Point out each leukocyte.
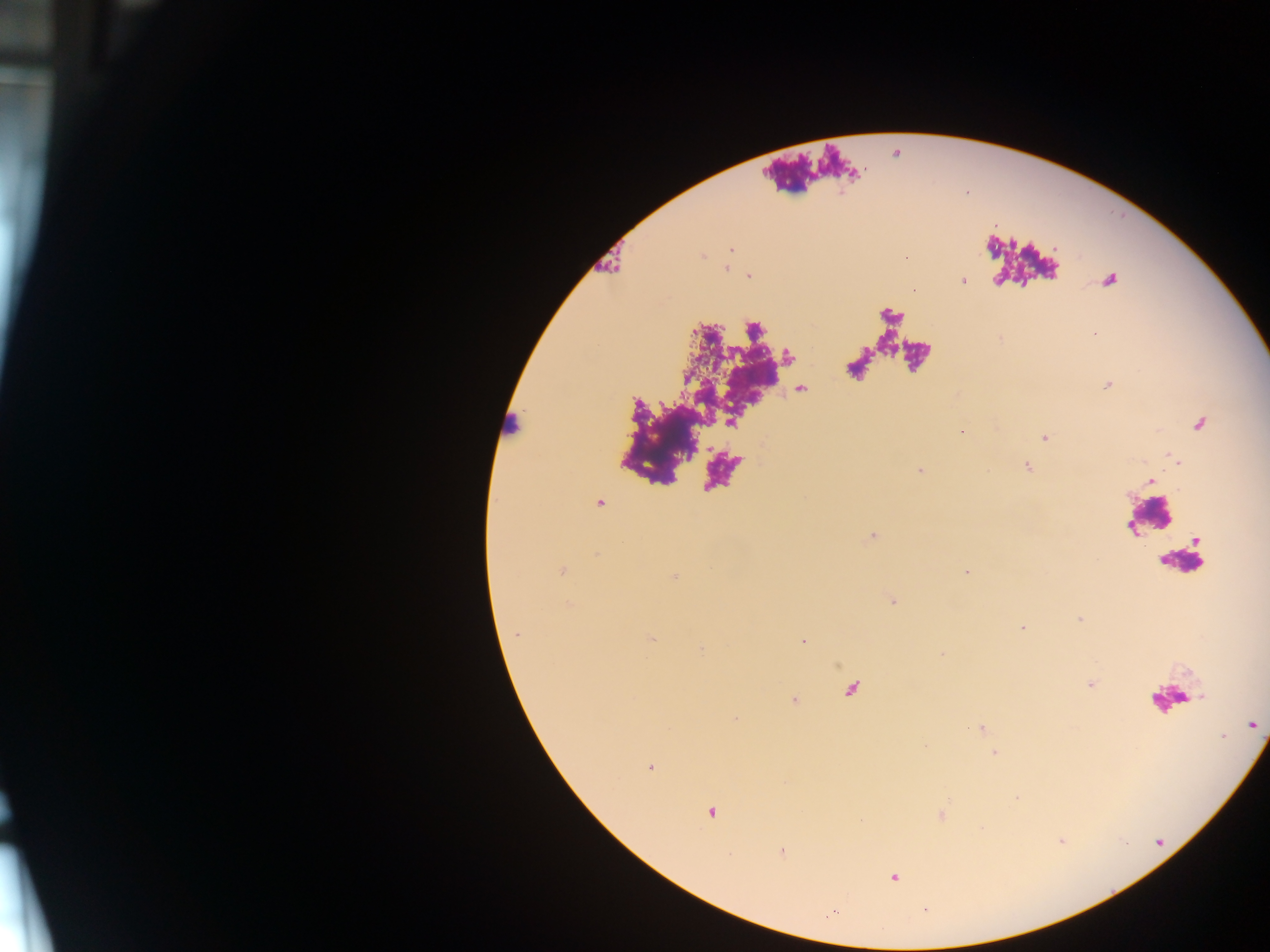

Approximate centers as {x, y} in pixels.
Leukocytes: {512, 427}, {1149, 517}, {1182, 561}, {1169, 699}.

Malaria parasite locations: {731, 248}, {726, 268}, {748, 275}, {962, 280}, {1107, 384}, {1200, 425}, {963, 431}, {1044, 437}, {1026, 466}, {919, 469}, {1150, 479}, {598, 502}, {872, 535}, {562, 571}, {966, 572}, {674, 576}, {892, 600}, {1022, 627}, {651, 638}, {803, 641}, {1091, 684}, {794, 701}, {1252, 724}, {980, 728}, {995, 752}, {650, 767}, {711, 811}, {941, 815}, {781, 851}, {893, 877}, {924, 909}, {833, 910}. Collected in Ghana. Thick blood film. Image is 1270×952 pixels. One field of view. Photographed through a microscope with a mobile-phone camera.